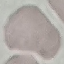

Summary:
  - Result: no malaria parasites seen
  - Capture: smartphone through the microscope eyepiece
  - Stain: Giemsa
  - Image type: cell patch, automatically extracted from a larger field of view and resized to 64 × 64 pixels
  - Preparation: thin blood film